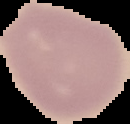
image type = cell region segmented out of the field of view; surrounding area masked to black
image size = 130×124 pixels
malaria status = uninfected
preparation = thin blood smear